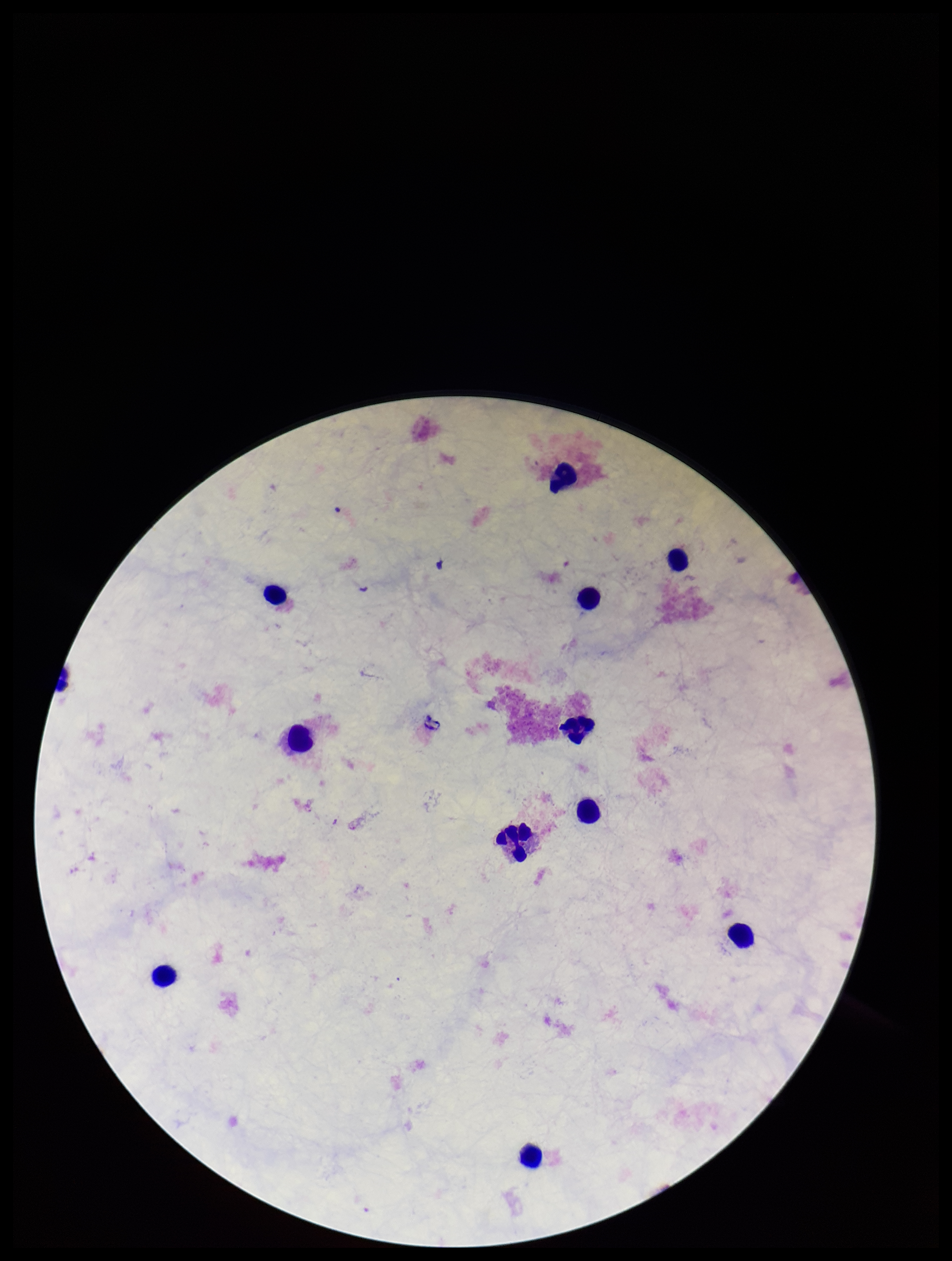

leukocyte_count: 11
image_size: 952×1261 pixels
capture: smartphone photograph through the microscope eyepiece
plasmodium_parasites: none identified
preparation: thick
stain: Giemsa
field_of_view: one from this slide
parasite_count: 0
patient_malaria_status: negative